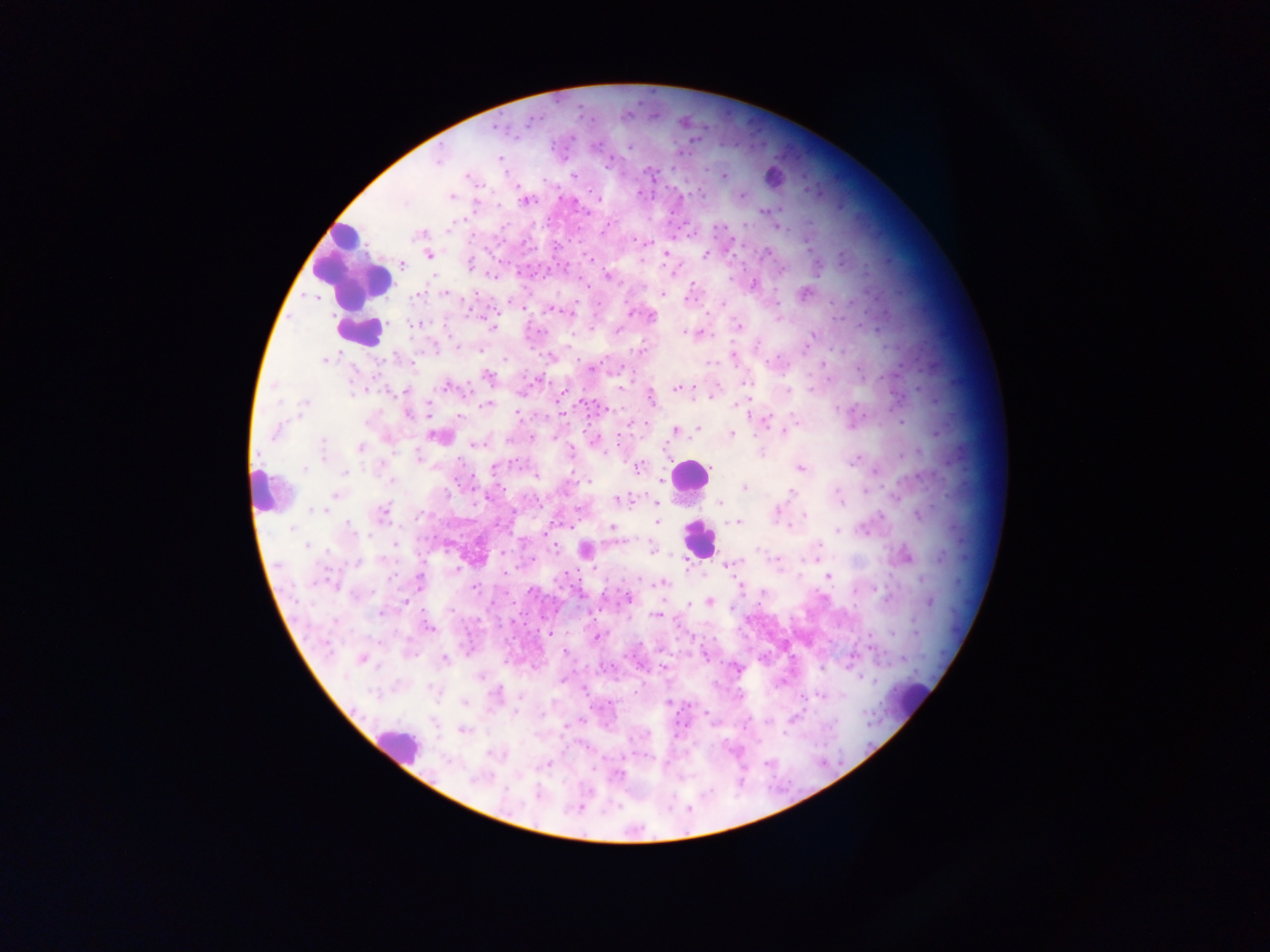

country = Ghana
preparation = thick blood smear
image size = 1270×952 pixels
malaria parasite locations = approximate centers as {x, y} in pixels: {531, 120}, {498, 127}, {630, 146}, {439, 158}, {499, 158}, {608, 164}, {649, 171}, {466, 175}, {572, 175}, {723, 175}, {741, 195}, {451, 196}, {598, 198}, {526, 201}, {764, 211}, {504, 226}, {449, 229}, {421, 235}, {633, 239}, {766, 252}, {667, 253}, {705, 254}, {429, 255}, {589, 257}, {640, 260}, {404, 263}, {470, 264}, {780, 270}, {672, 271}, {607, 276}, {730, 279}, {693, 284}, {754, 284}, {446, 293}, {803, 293}, {419, 294}, {663, 294}, {687, 298}, {723, 304}, {554, 310}, {631, 312}, {652, 317}, {779, 319}, {414, 325}, {738, 326}, {493, 328}, {540, 331}, {618, 331}, {685, 332}, {812, 335}, {810, 339}, {434, 345}, {757, 346}, {457, 347}, {804, 347}, {639, 350}, {332, 357}, {733, 357}, {325, 359}, {711, 362}, {823, 363}, {593, 368}, {488, 376}, {446, 386}, {621, 387}, {678, 388}, {390, 390}, {787, 390}, {406, 391}, {651, 397}, {711, 397}, {304, 404}, {486, 404}, {739, 404}, {837, 408}, {519, 413}, {407, 414}, {561, 414}, {459, 416}, {766, 419}, {902, 422}, {697, 429}, {676, 430}, {276, 432}, {784, 432}, {937, 433}, {732, 434}, {436, 435}, {531, 437}, {553, 438}, {594, 440}, {618, 440}, {476, 444}, {324, 447}, {361, 448}, {918, 451}, {761, 452}, {323, 456}, {418, 458}, {853, 462}, {514, 463}, {639, 466}, {800, 468}, {304, 469}, {494, 469}, {874, 470}, {346, 471}, {536, 476}, {389, 480}, {589, 482}, {662, 482}, {744, 488}, {837, 491}, {864, 491}, {791, 493}, {335, 494}, {619, 500}, {655, 503}, {720, 503}, {312, 509}, {319, 509}, {383, 511}, {776, 511}, {880, 515}, {805, 516}, {919, 516}, {736, 522}, {656, 523}, {350, 526}, {613, 527}, {789, 527}, {291, 529}, {838, 532}, {395, 544}, {819, 544}, {307, 546}, {555, 547}, {652, 547}, {758, 549}, {585, 550}, {907, 556}, {941, 557}, {777, 560}, {356, 562}, {729, 564}, {456, 569}, {505, 573}, {829, 577}, {922, 580}, {420, 581}, {661, 584}, {333, 586}, {474, 588}, {531, 591}, {626, 597}, {710, 601}, {930, 602}, {404, 603}, {689, 603}, {381, 613}, {655, 615}, {428, 627}, {915, 628}, {549, 634}, {893, 634}, {596, 637}, {869, 637}, {565, 652}, {361, 659}, {444, 659}, {903, 659}, {664, 668}, {497, 691}, {820, 696}, {464, 703}, {668, 704}, {514, 711}, {793, 718}, {463, 731}, {548, 763}, {477, 779}, {537, 794}
field of view = single
leukocyte locations = approximate centers as {x, y} in pixels: {773, 177}, {352, 264}, {360, 330}, {689, 475}, {264, 489}, {700, 539}, {914, 699}, {397, 744}
capture = mobile-phone photograph through a microscope